Assess this cell for malaria.
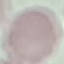
It is uninfected.

Summary:
  - Preparation: thin smear
  - Capture: smartphone camera at the microscope eyepiece
  - Image type: automatically extracted cell patch, resized to 64 × 64 pixels
  - Stain: Giemsa